State which parasite is depicted.
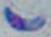
This is Toxoplasma gondii.

Summary:
  - Modality: photomicrograph
  - Magnification: 1000x